Report the malaria status of this cell.
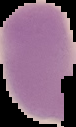
Uninfected.

Image is 76×127 pixels. Segmented cell region on a black background. From a thin blood smear.